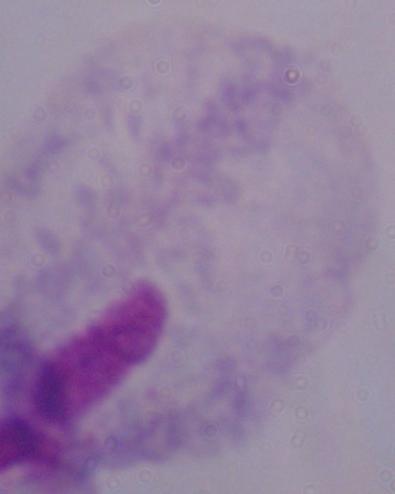
Captured at 1000x magnification. A trichomonad is seen. Micrograph.